Draw a bounding box around every malaria parasite.
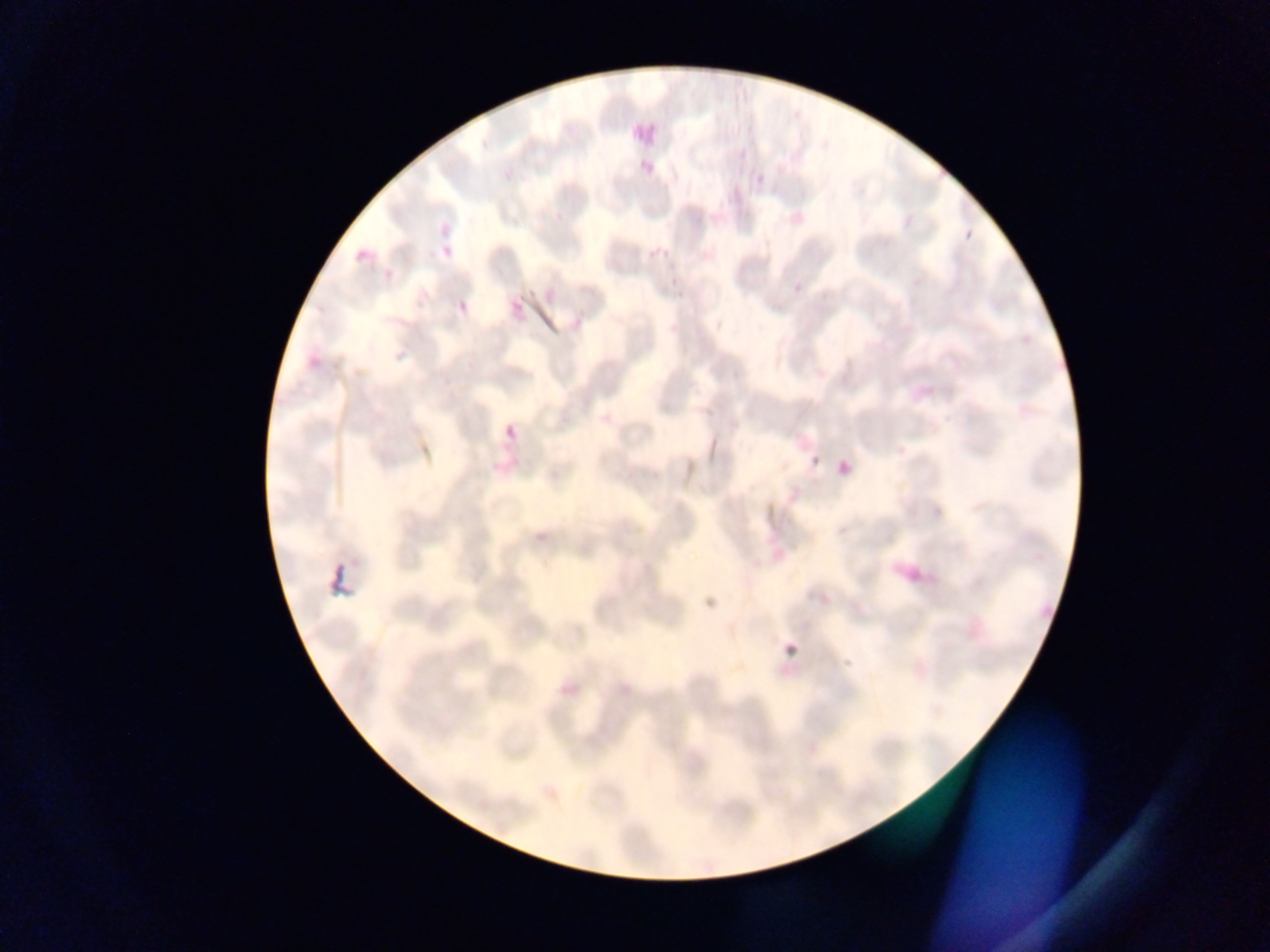

Approximate bounding boxes as [left, top, right, bottom] in pixels.
Malaria parasites: [434, 215, 449, 238], [965, 230, 974, 240], [340, 240, 381, 262], [440, 241, 463, 260], [377, 268, 400, 285], [792, 284, 803, 295], [457, 286, 477, 319], [508, 298, 525, 318], [501, 406, 531, 444], [811, 454, 823, 466], [836, 459, 853, 477], [839, 525, 850, 537], [784, 642, 799, 657].

Summary:
  - Country: Ghana
  - Preparation: thin blood smear
  - Image size: 1270×952 pixels
  - Field of view: single
  - Capture: mobile-phone photograph through a microscope